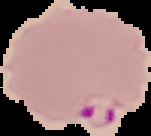
Summary:
  - Preparation: thin blood smear
  - Malaria status: parasitized
  - Image type: segmented cell region with the area outside set to black
  - Image size: 151×136 pixels